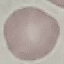
Summary:
  - Malaria status: uninfected
  - Stain: Giemsa
  - Preparation: thin smear
  - Image type: automatically extracted cell patch, resized to 64 × 64 pixels
  - Capture: smartphone camera at the microscope eyepiece